Outline each uninfected red blood cell.
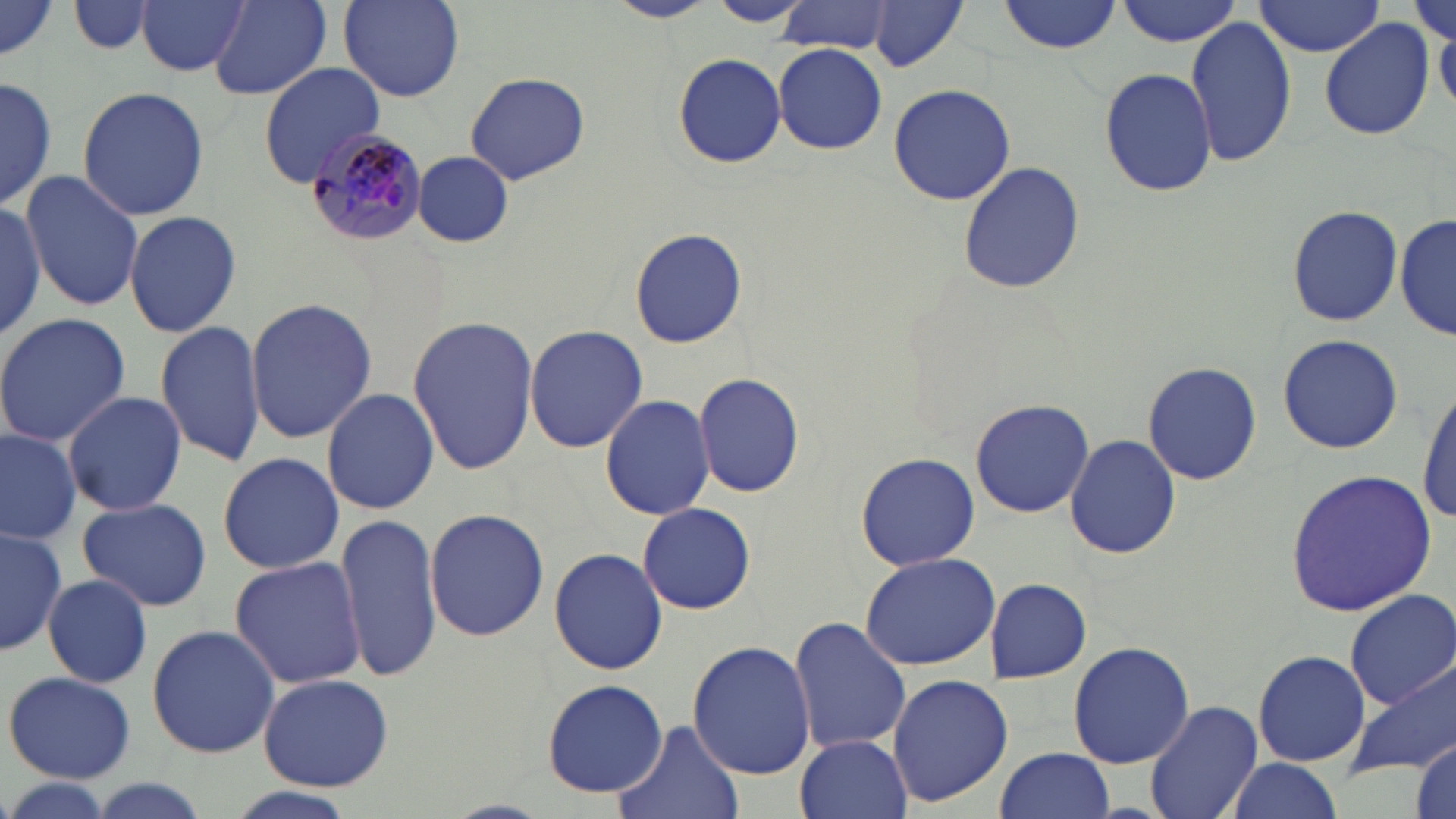
Approximate bounding boxes as (x1,y1)-(x2,y2) corner pairs in pixels.
Uninfected red blood cells: (135,0)-(250,78), (607,0)-(717,23), (1000,0)-(1124,54), (1116,0)-(1245,46), (66,1)-(158,56), (210,1)-(333,99), (338,1)-(465,103), (707,1)-(808,26), (864,1)-(970,73), (1253,1)-(1389,57), (1407,2)-(1454,50), (0,3)-(59,65), (777,4)-(899,56), (1185,15)-(1297,167), (1320,21)-(1434,141), (1435,25)-(1455,110), (772,44)-(887,154), (673,52)-(787,168), (258,62)-(387,187), (1100,65)-(1215,197), (464,73)-(591,183), (0,77)-(56,212), (886,83)-(1018,206), (76,87)-(211,220), (411,151)-(515,249), (955,161)-(1089,294), (19,170)-(145,312), (0,194)-(47,349), (0,203)-(48,341), (1286,205)-(1404,327), (124,210)-(243,339), (1397,210)-(1454,343), (629,226)-(747,351), (246,297)-(376,443), (0,312)-(131,448), (407,314)-(539,478), (155,318)-(265,467), (524,324)-(649,451), (1277,333)-(1403,456), (1142,359)-(1263,485), (695,372)-(806,500), (321,387)-(440,514), (1416,388)-(1455,524), (62,390)-(187,516), (599,393)-(716,521), (969,397)-(1095,519), (0,428)-(81,546), (1064,432)-(1179,560), (854,451)-(980,571), (216,452)-(343,573), (1284,469)-(1435,615), (75,496)-(213,612), (637,502)-(756,614), (424,507)-(550,643), (335,513)-(444,685), (0,525)-(65,659), (550,548)-(667,675), (860,552)-(1000,671), (228,555)-(369,688), (44,574)-(153,688), (986,578)-(1091,682), (1344,588)-(1455,708), (788,616)-(912,758), (146,624)-(279,759), (687,641)-(817,779), (1067,641)-(1194,768), (1252,649)-(1371,768), (1347,660)-(1456,777), (4,670)-(137,783), (256,672)-(394,790), (887,673)-(1013,808), (542,680)-(665,797), (1144,699)-(1263,819), (613,719)-(744,819), (796,733)-(912,819), (1411,737)-(1454,819), (995,747)-(1114,819), (1227,758)-(1342,817), (0,778)-(115,819), (82,778)-(213,819), (218,784)-(361,819).

Summary:
  - Plasmodium malariae-infected red blood cell locations: (301,127)-(428,245)
  - Slide-level diagnosis: Plasmodium malariae
  - Preparation: thin blood smear
  - Stain: May-Grünwald-Giemsa
  - Image size: 1456×819 pixels
  - Magnification: 1000x
  - Field of view: one of a larger specimen
  - Modality: light microscopy